Outline each blood parasite and name the species.
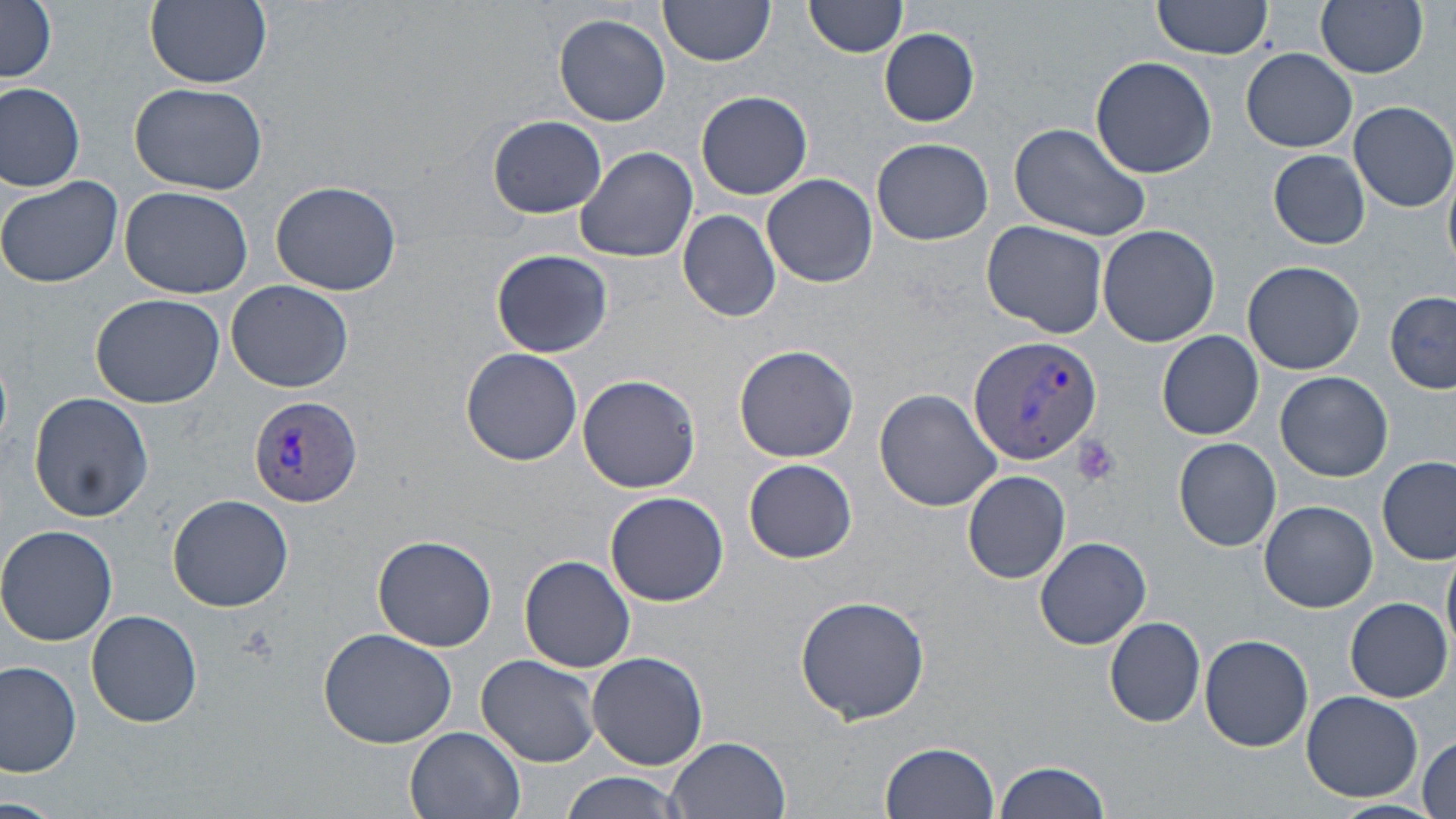

Approximate bounding boxes as (x1, y1, x2, y2) in pixels.
Plasmodium vivax-infected red blood cells: (967, 334, 1102, 467), (249, 395, 363, 508).
No Plasmodium falciparum, Plasmodium ovale, Plasmodium malariae, Babesia divergens, or Trypanosoma brucei observed.

Platelet locations: (1071, 435, 1120, 486). Uninfected red blood cell locations: (2, 0, 58, 83), (144, 0, 272, 88), (659, 0, 776, 66), (803, 0, 908, 58), (1147, 0, 1276, 64), (1316, 0, 1428, 78), (554, 12, 671, 127), (879, 28, 979, 127), (1242, 48, 1357, 152), (1089, 56, 1217, 177), (130, 82, 267, 196), (0, 83, 85, 193), (696, 90, 813, 200), (1350, 101, 1455, 211), (486, 114, 608, 219), (1011, 120, 1152, 241), (872, 137, 993, 246), (574, 145, 697, 261), (1269, 149, 1371, 248), (1443, 159, 1456, 272), (762, 174, 877, 287), (0, 175, 123, 288), (270, 181, 401, 296), (120, 186, 254, 299), (678, 210, 782, 322), (982, 218, 1110, 338), (1097, 225, 1221, 349), (490, 248, 613, 359), (1242, 260, 1365, 375), (224, 280, 354, 392), (1385, 290, 1456, 395), (90, 293, 226, 406), (1157, 330, 1263, 439), (733, 344, 859, 463), (460, 348, 583, 466), (1276, 372, 1390, 482), (576, 374, 704, 495), (874, 388, 1003, 512), (29, 392, 154, 522), (1174, 437, 1282, 551), (1378, 457, 1454, 565), (743, 458, 856, 563), (963, 470, 1071, 584), (605, 491, 729, 605), (167, 495, 294, 611), (1259, 501, 1378, 612), (0, 526, 120, 647), (371, 535, 498, 652), (1031, 535, 1153, 650), (519, 555, 636, 673), (795, 595, 931, 723), (1345, 598, 1451, 701), (86, 609, 203, 729), (1104, 615, 1207, 727), (318, 626, 460, 750), (1199, 634, 1316, 753), (588, 650, 708, 770), (477, 654, 601, 768), (0, 661, 81, 778), (1300, 689, 1423, 802), (405, 726, 526, 819), (1417, 735, 1454, 819), (665, 737, 791, 819), (881, 740, 1001, 819), (994, 759, 1112, 819), (559, 771, 690, 819), (0, 797, 61, 818), (1327, 800, 1452, 819). Slide-level diagnosis: Plasmodium vivax. May-Grünwald-Giemsa stain. Image is 1456×819 pixels. Thin blood film. Light microscopy. 1000x magnification. One field of a larger specimen.